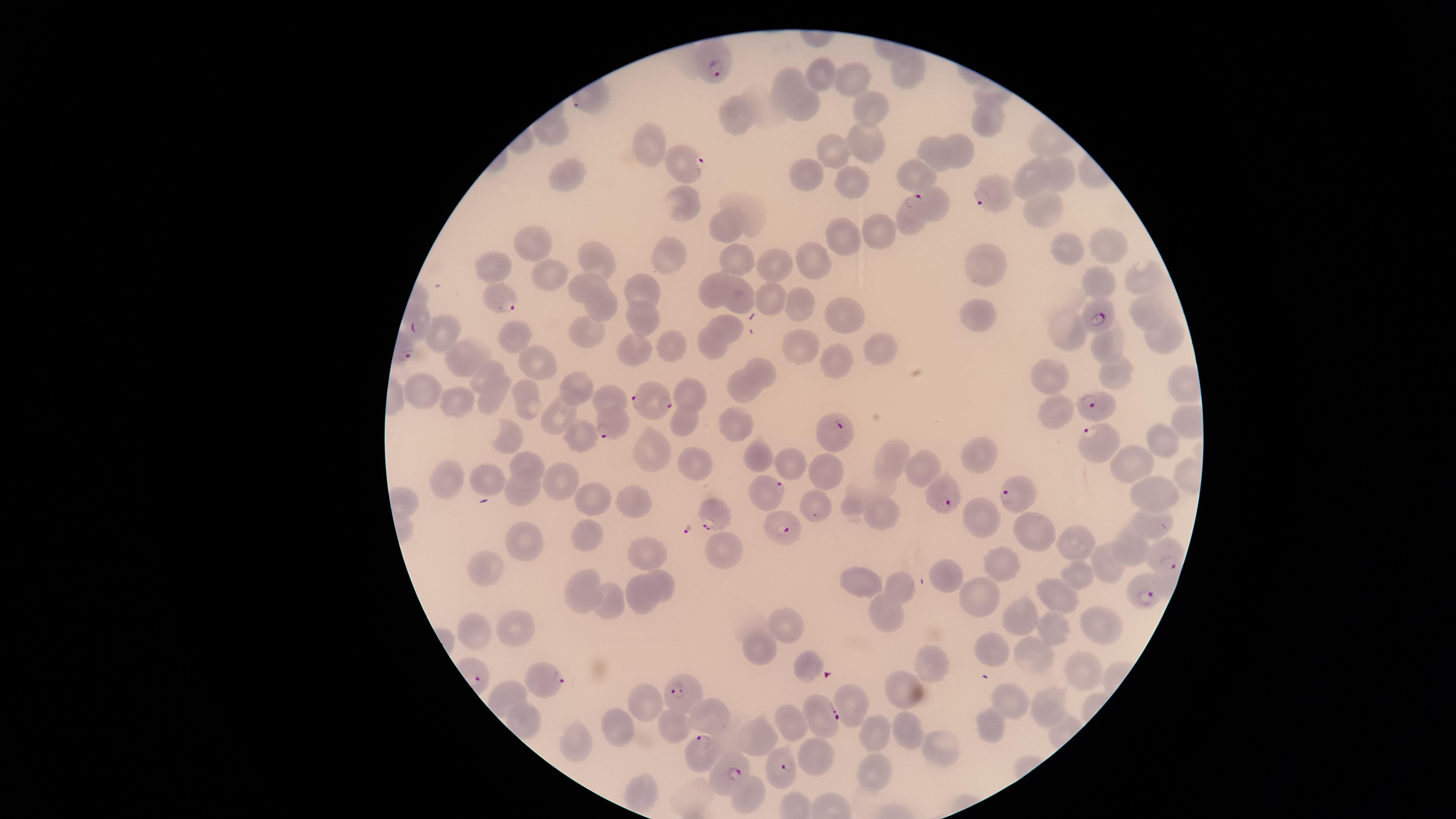
parasitized_red_blood_cells: 'approximate marker points as (x, y) in pixels: (714, 65), (687, 166), (990, 198), (912, 207), (502, 298), (1094, 317), (417, 326), (660, 405), (1097, 408), (620, 422), (838, 427), (1093, 436), (768, 488), (1014, 491), (945, 494), (715, 513), (782, 526), (1161, 553), (1139, 595), (548, 681), (679, 689), (817, 712), (697, 751), (789, 766), (734, 771)'
visible_region: circular
presence: malaria parasites seen
species: Plasmodium falciparum
uninfected_red_blood_cells: 'approximate marker points as (x, y) in pixels: (908, 71), (818, 73), (786, 76), (854, 77), (808, 107), (868, 107), (738, 114), (985, 121), (551, 131), (648, 139), (866, 139), (957, 147), (837, 149), (939, 152), (807, 172), (917, 173), (1026, 174), (1057, 176), (573, 182), (848, 183), (937, 205), (746, 206), (1038, 206), (685, 210), (881, 226), (728, 227), (842, 237), (535, 240), (1102, 247), (1071, 250), (600, 257), (671, 257), (815, 259), (742, 260), (774, 263), (986, 266), (485, 271), (549, 276), (1095, 280), (1142, 282), (586, 286), (716, 287), (644, 290), (741, 294), (771, 300), (800, 305), (605, 307), (1144, 312), (837, 313), (645, 316), (983, 316), (730, 328), (444, 330), (1069, 330), (515, 332), (587, 335), (1156, 337), (1107, 341), (710, 344), (796, 345), (877, 345), (667, 348), (635, 352), (488, 353), (534, 355), (463, 358), (838, 363), (490, 371), (760, 373), (1051, 375), (1114, 375), (1180, 381), (746, 388), (578, 390), (427, 391), (691, 391), (526, 397), (494, 398), (613, 399), (460, 400), (1053, 408), (561, 415), (685, 418), (736, 421), (1184, 424), (577, 433), (1157, 436), (507, 439), (649, 453), (761, 455), (986, 455), (792, 461), (898, 461), (1132, 461), (696, 462), (922, 464), (529, 467), (821, 473), (444, 479), (490, 479), (561, 479), (520, 489), (1160, 491), (632, 500), (588, 501), (808, 505), (855, 506), (880, 512), (979, 517), (1149, 520), (1037, 528), (585, 537), (527, 539), (1079, 546), (724, 548), (1130, 549), (652, 555), (1006, 560), (490, 565), (1113, 565), (948, 576), (1083, 576), (854, 578), (660, 583), (904, 586), (643, 588), (580, 589), (1058, 594), (976, 595), (610, 602), (892, 611), (1020, 620), (1096, 623), (783, 627), (512, 628), (476, 631), (1056, 631), (759, 648), (992, 652), (932, 660), (1035, 662), (810, 666), (1076, 667), (907, 689), (1011, 702), (644, 703), (851, 707), (1048, 707), (709, 715), (796, 722), (994, 723), (669, 726), (618, 728), (906, 730), (874, 732), (578, 737), (764, 740), (942, 745), (822, 755), (874, 768), (643, 792), (750, 793)'
stain: Giemsa
preparation: thin blood smear
field_of_view: single
capture: smartphone photograph through the microscope eyepiece
image_size: 1456×819 pixels